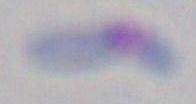 Photomicrograph. Toxoplasma gondii is seen. 1000x magnification.